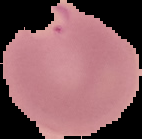 From a thin blood film. Malaria status: parasitized. Image is 142×139 pixels. Cell region segmented out of the field of view; the surrounding area is masked to black.